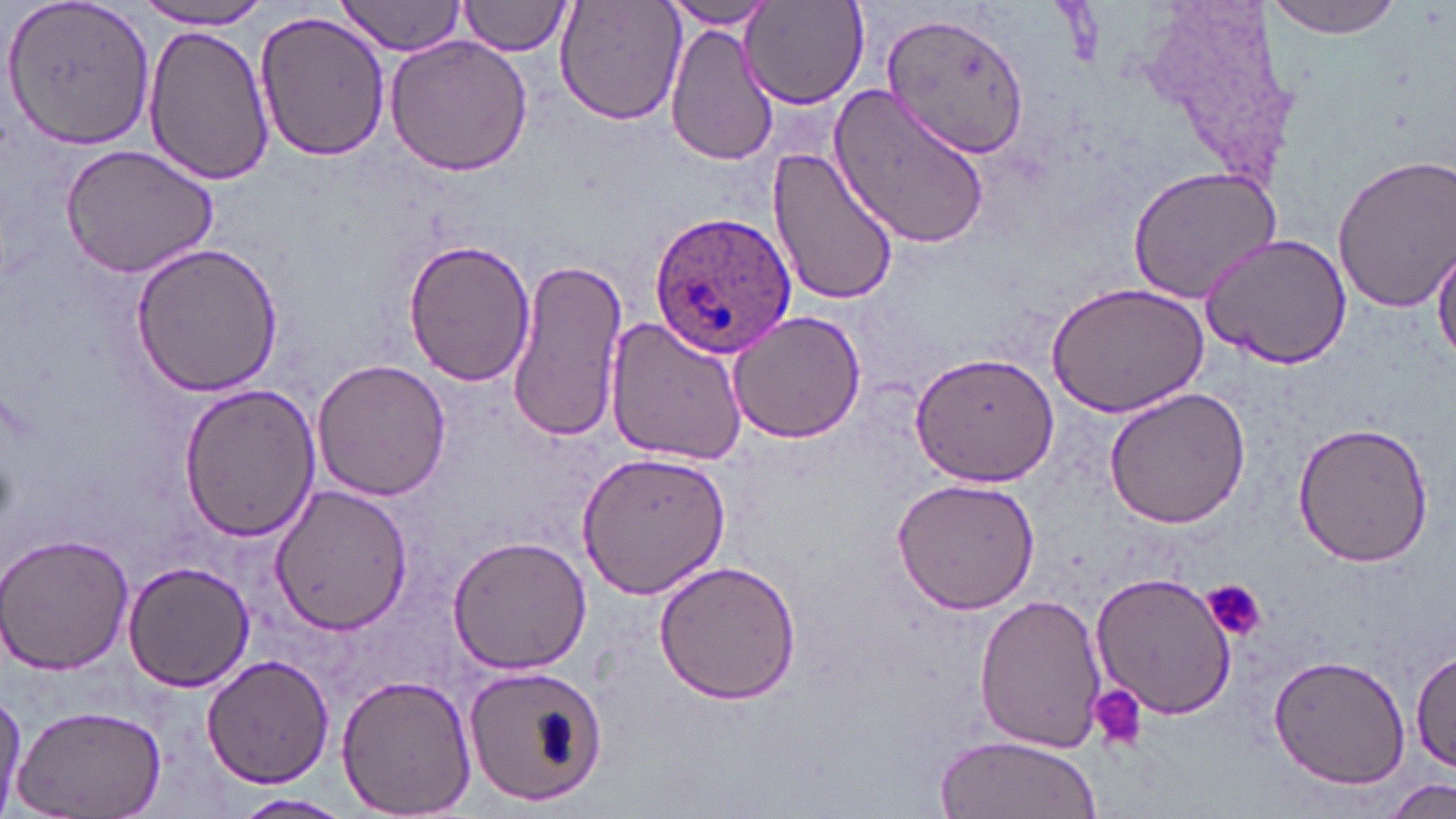
slide-level diagnosis = Plasmodium ovale
stain = May-Grünwald-Giemsa
Plasmodium ovale-infected red blood cell locations = approximate bounding boxes as (x1, y1, x2, y2) in pixels: (647, 209, 799, 361)
field of view = single
uninfected red blood cell locations = approximate bounding boxes as (x1, y1, x2, y2) in pixels: (334, 0, 468, 57), (459, 0, 574, 57), (555, 0, 686, 126), (657, 0, 785, 29), (739, 0, 870, 109), (1261, 0, 1406, 39), (3, 1, 156, 148), (132, 1, 280, 31), (878, 8, 1030, 161), (254, 10, 389, 164), (665, 22, 776, 169), (144, 24, 273, 185), (384, 36, 534, 176), (830, 83, 992, 251), (60, 143, 219, 279), (768, 148, 897, 310), (1329, 151, 1456, 315), (1128, 164, 1283, 304), (1200, 232, 1352, 369), (403, 238, 535, 386), (130, 243, 283, 396), (1433, 243, 1456, 364), (506, 258, 628, 444), (1047, 282, 1207, 418), (725, 309, 869, 445), (605, 317, 748, 466), (910, 350, 1060, 487), (311, 359, 452, 503), (177, 383, 320, 541), (1102, 385, 1250, 528), (1291, 419, 1433, 568), (571, 450, 730, 599), (887, 477, 1038, 615), (270, 482, 411, 633), (0, 533, 133, 675), (447, 534, 593, 672), (122, 558, 256, 690), (652, 560, 803, 705), (1090, 569, 1237, 721), (971, 591, 1110, 752), (1413, 648, 1454, 772), (1268, 654, 1409, 789), (200, 656, 335, 790), (463, 663, 603, 806), (336, 672, 477, 818), (0, 687, 25, 816), (11, 702, 167, 817), (935, 736, 1100, 819), (1387, 779, 1452, 818), (230, 794, 353, 818)
preparation = thin blood smear
platelet locations = approximate bounding boxes as (x1, y1, x2, y2) in pixels: (1204, 580, 1267, 639), (1088, 686, 1149, 752)
image size = 1456×819 pixels
magnification = 1000x
modality = light microscopy